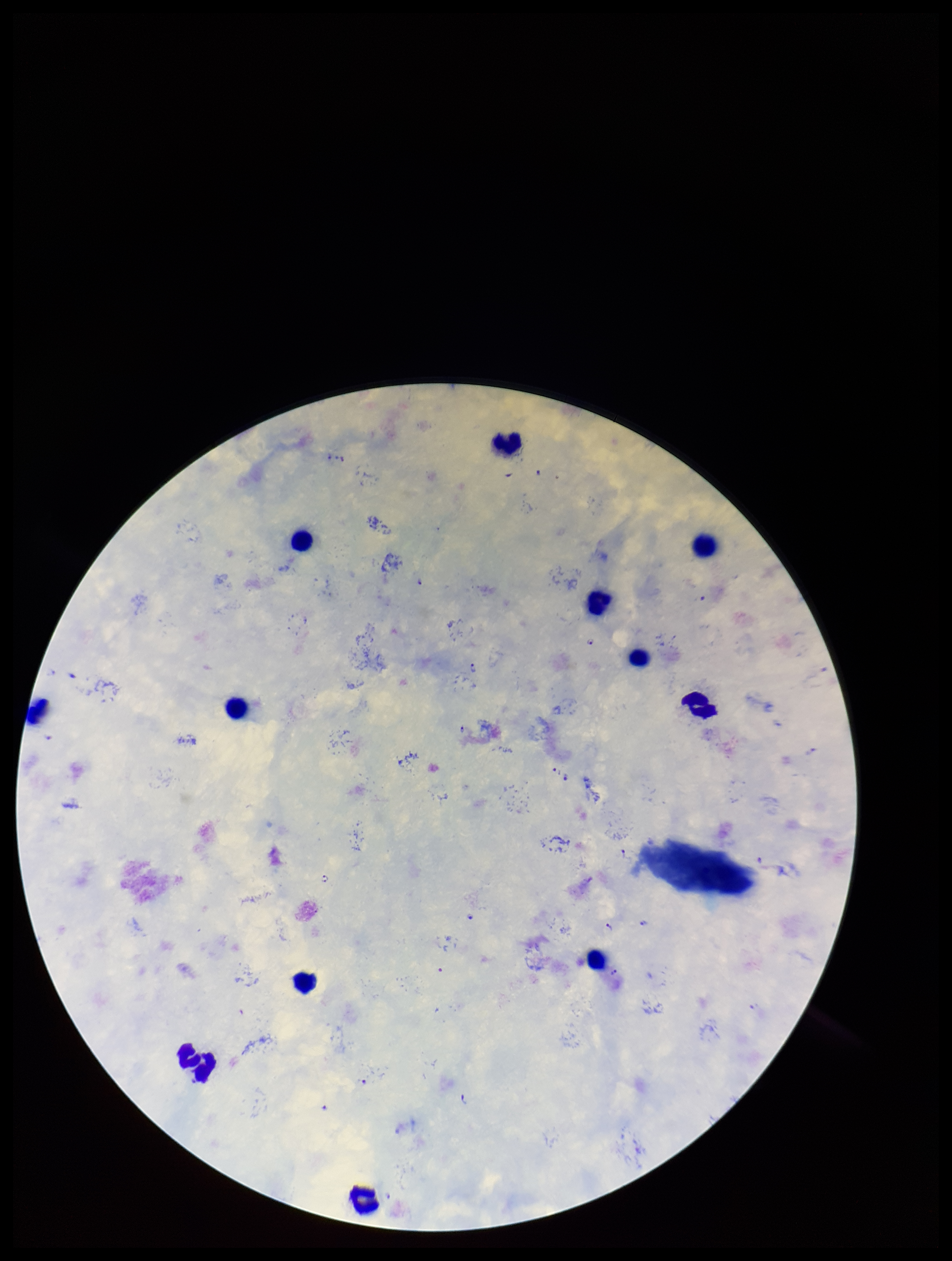
parasite count = 12
leukocyte count = 12
image size = 952×1261 pixels
stain = Giemsa
field of view = single
preparation = thick blood smear
Plasmodium parasites = seen
species reported for this patient = Plasmodium falciparum
capture = smartphone photograph through the microscope eyepiece
patient malaria status = infected